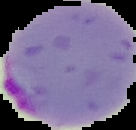

Summary:
  - Malaria status: parasitized
  - Image type: segmented cell region with the area outside set to black
  - Preparation: thin blood smear
  - Image size: 136×130 pixels